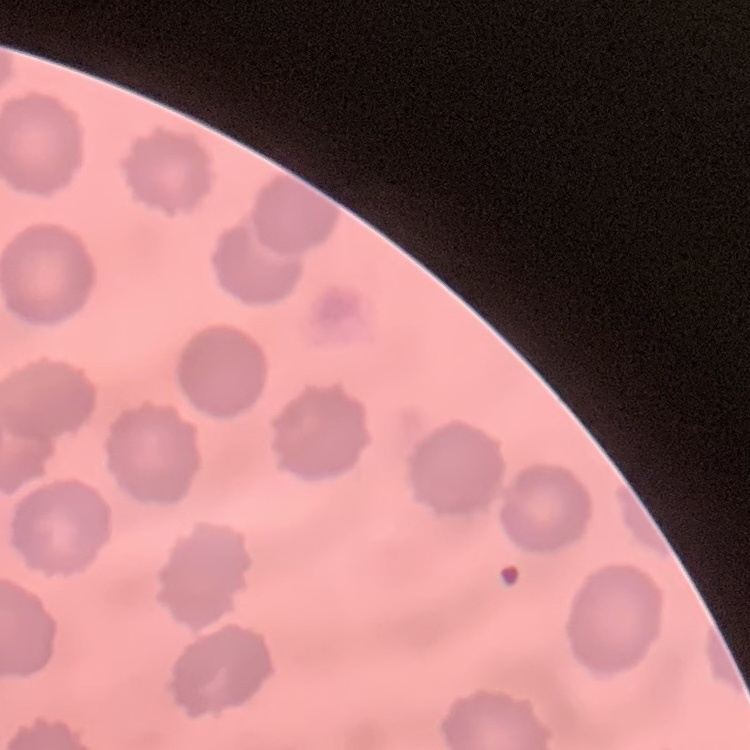
The red blood cells show no rouleaux formation. Thin blood film. One tile cut from a larger photomicrograph. Field's or Giemsa stain.